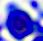
{
  "magnification": "400x",
  "identification": "white blood cell",
  "modality": "micrograph"
}